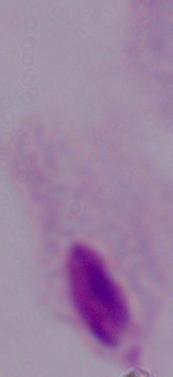
Summary:
  - Modality: photomicrograph
  - Identification: trichomonad
  - Magnification: 1000x